Locate platelets.
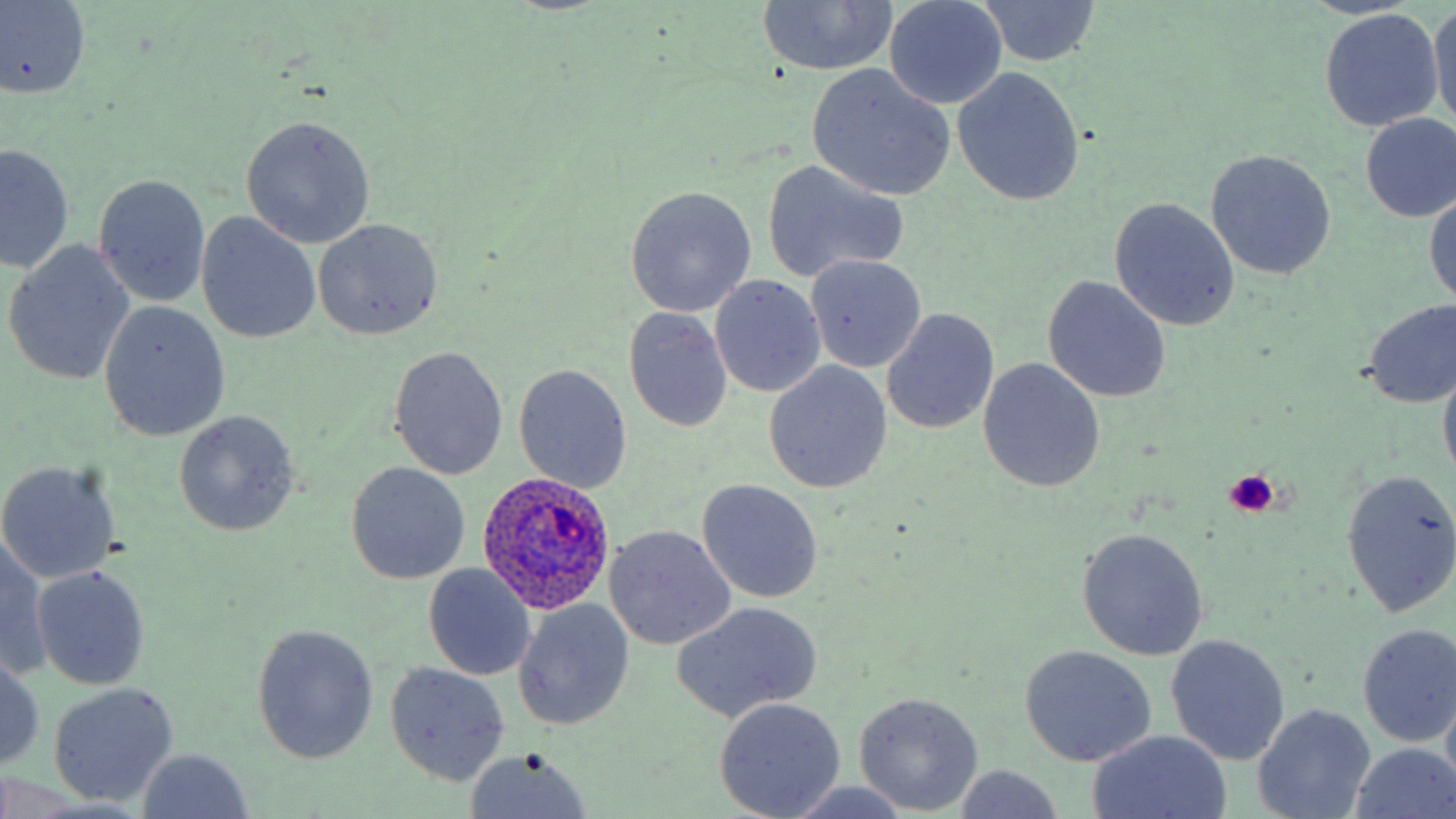
Approximate bounding boxes as [x1, y1, x2, y2] in pixels.
Platelets: [1222, 469, 1279, 517].

Summary:
  - Plasmodium ovale-infected red blood cell locations: [478, 471, 618, 613]
  - Uninfected red blood cell locations: [1, 0, 93, 98], [884, 0, 1007, 109], [977, 1, 1103, 67], [1429, 1, 1455, 131], [755, 2, 899, 75], [1318, 9, 1446, 131], [807, 65, 955, 199], [952, 65, 1085, 206], [1358, 112, 1456, 222], [239, 115, 375, 249], [1, 143, 73, 275], [1205, 149, 1337, 280], [760, 159, 910, 283], [93, 174, 211, 306], [624, 185, 757, 318], [1425, 188, 1456, 312], [1107, 198, 1241, 331], [198, 213, 321, 344], [312, 218, 443, 341], [4, 240, 136, 384], [805, 254, 926, 373], [709, 275, 826, 398], [1042, 276, 1173, 403], [101, 300, 230, 441], [1360, 300, 1456, 408], [624, 307, 734, 432], [882, 308, 998, 435], [388, 345, 509, 479], [978, 358, 1105, 493], [1438, 359, 1456, 486], [764, 362, 892, 493], [513, 364, 633, 493], [174, 410, 300, 537], [0, 460, 120, 585], [344, 462, 471, 584], [1339, 469, 1456, 619], [697, 479, 824, 603], [604, 525, 735, 649], [1077, 527, 1209, 660], [1, 537, 49, 678], [422, 563, 536, 682], [31, 564, 151, 689], [514, 600, 634, 730], [674, 602, 823, 720], [251, 623, 380, 764], [1356, 624, 1456, 746], [1165, 634, 1290, 765], [1018, 644, 1157, 767], [0, 653, 45, 769], [383, 663, 510, 786], [47, 683, 180, 807], [853, 692, 984, 815], [715, 697, 846, 817], [1252, 703, 1375, 819], [1086, 731, 1232, 819], [1350, 743, 1456, 818], [137, 750, 254, 817], [464, 750, 593, 819], [952, 764, 1068, 819], [777, 781, 918, 819]
  - Slide-level diagnosis: Plasmodium ovale
  - Field of view: single
  - Magnification: 1000x
  - Preparation: thin blood film
  - Stain: May-Grünwald-Giemsa
  - Modality: light microscopy
  - Image size: 1456×819 pixels